Outline each blood parasite and name the species.
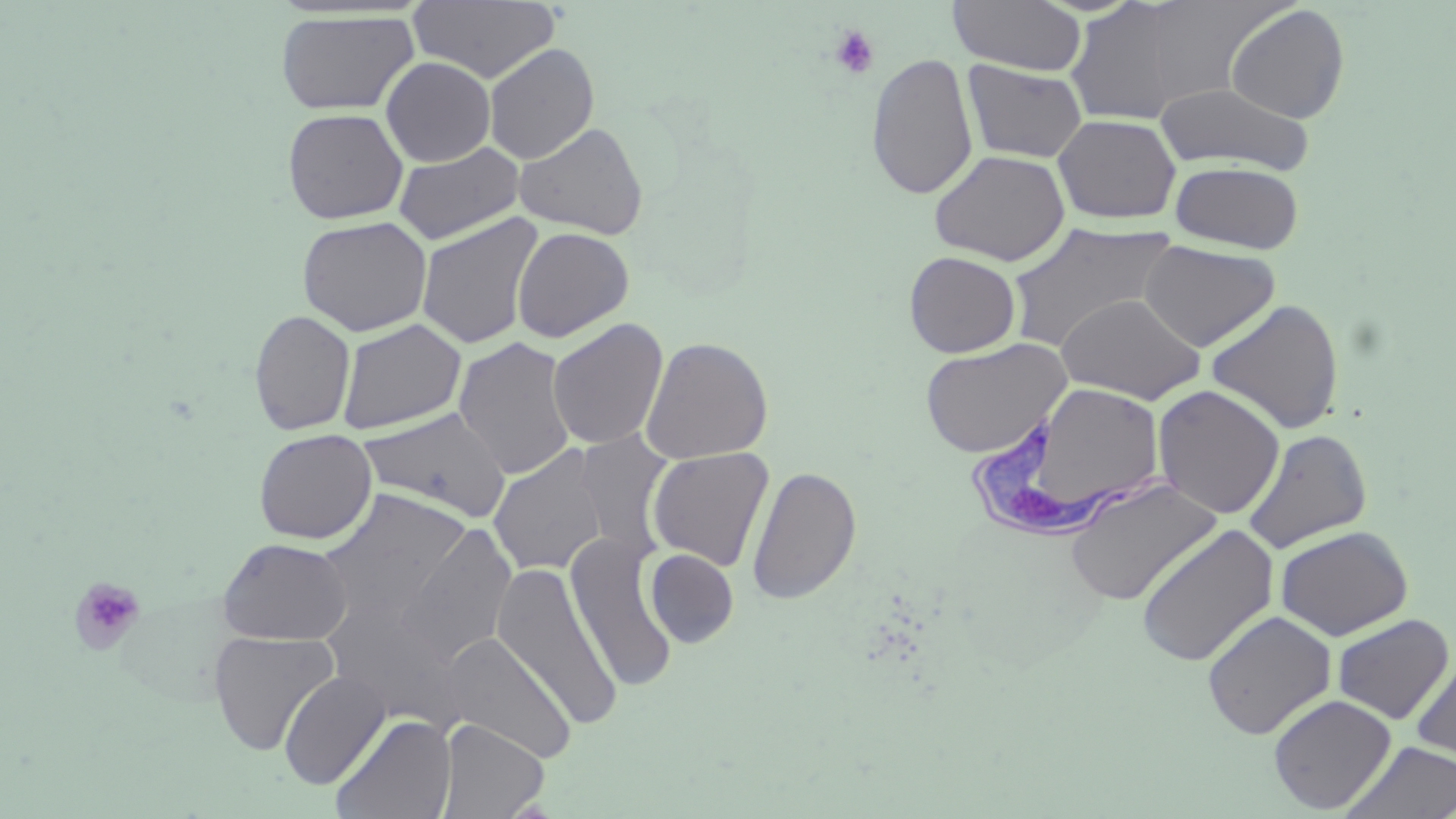
Approximate bounding boxes as (x1, y1, x2, y2) in pixels.
Trypanosoma brucei: (958, 415, 1184, 541).
No Plasmodium falciparum, Plasmodium ovale, Plasmodium malariae, Plasmodium vivax, or Babesia divergens observed.

Platelet locations: (829, 25, 880, 80), (69, 576, 146, 656). Uninfected red blood cell locations: (410, 0, 561, 83), (1064, 0, 1207, 124), (948, 1, 1087, 76), (1225, 4, 1350, 124), (274, 10, 419, 116), (483, 42, 600, 164), (866, 52, 979, 200), (380, 56, 496, 167), (962, 60, 1088, 163), (1154, 82, 1316, 176), (282, 107, 408, 224), (1052, 114, 1181, 225), (514, 121, 649, 240), (393, 141, 525, 246), (928, 149, 1070, 266), (1170, 161, 1304, 253), (416, 212, 544, 350), (296, 215, 433, 336), (1005, 220, 1177, 352), (512, 226, 634, 342), (1139, 239, 1280, 352), (904, 251, 1021, 358), (1056, 292, 1206, 404), (1206, 299, 1345, 434), (249, 308, 356, 435), (336, 318, 467, 435), (547, 318, 669, 451), (453, 336, 577, 481), (640, 336, 773, 465), (919, 338, 1071, 458), (993, 382, 1169, 531), (1152, 384, 1286, 520), (357, 407, 512, 524), (253, 428, 377, 544), (1242, 428, 1373, 553), (573, 430, 675, 558), (488, 445, 609, 576), (647, 447, 774, 572), (746, 465, 862, 606), (1064, 477, 1223, 607), (318, 489, 472, 626), (397, 522, 518, 669), (1134, 523, 1279, 667), (1275, 526, 1414, 640), (565, 533, 679, 693), (216, 537, 353, 646), (644, 548, 738, 648), (492, 561, 622, 732), (322, 591, 467, 727), (1202, 610, 1336, 740), (1331, 614, 1454, 724), (208, 629, 339, 756), (440, 632, 576, 763), (1410, 651, 1456, 767), (278, 671, 389, 790), (1268, 694, 1396, 814), (330, 712, 456, 819), (437, 718, 550, 818), (1341, 740, 1456, 819). Slide-level diagnosis: Trypanosoma brucei. Thin blood film. One field of a larger specimen. May-Grünwald-Giemsa-stained preparation. Image is 1456×819 pixels. 1000x magnification. Optical microscopy.